Locate every malaria parasite and every leukocyte.
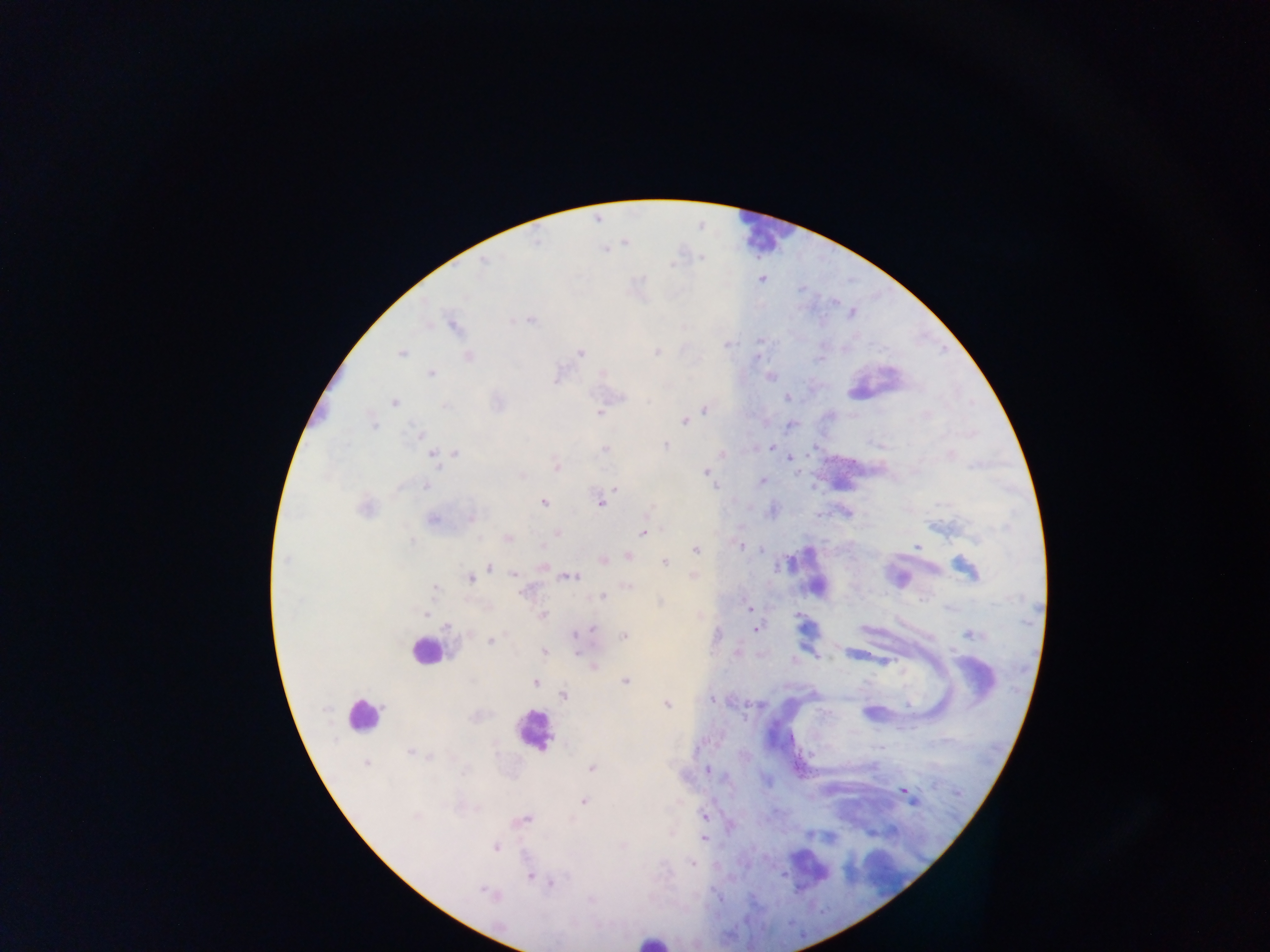

Approximate centers as (x, y) in pixels.
Malaria parasites: (536, 241), (484, 262), (761, 279), (531, 320), (453, 326), (726, 345), (656, 352), (401, 353), (581, 353), (468, 356), (820, 359), (431, 373), (603, 373), (770, 377), (623, 397), (787, 397), (395, 403), (446, 405), (704, 410), (600, 413), (684, 421), (374, 424), (419, 434), (665, 445), (772, 447), (605, 449), (456, 454), (434, 457), (791, 457), (557, 467), (706, 472), (762, 481), (426, 485), (615, 489), (543, 502), (600, 504), (365, 508), (472, 517), (433, 519), (557, 533), (643, 533), (508, 538), (412, 541), (740, 546), (918, 546), (760, 549), (696, 550), (628, 557), (286, 560), (603, 560), (665, 562), (489, 566), (966, 568), (513, 573), (569, 577), (470, 578), (628, 586), (435, 588), (526, 591), (603, 597), (749, 609), (425, 614), (543, 615), (447, 626), (592, 628), (756, 628), (973, 634), (625, 636), (491, 640), (544, 651), (593, 666), (625, 681), (535, 682), (564, 696), (711, 699), (667, 704), (410, 752), (429, 757), (366, 763), (592, 768), (708, 770), (903, 791), (909, 797), (583, 801), (704, 816), (416, 817), (526, 819), (703, 839), (496, 847), (693, 864), (530, 876), (551, 882), (486, 892).
Leukocytes: (765, 233), (424, 652), (360, 715), (532, 731), (652, 940).

Sample from Ghana. Thick blood smear. Mobile-phone photograph taken through the microscope. Image is 1270×952 pixels. Single field of view.